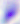

Summary:
  - Modality: photomicrograph
  - Identification: Toxoplasma gondii
  - Magnification: 400x